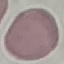

result = negative for malaria parasites
image type = cell patch, automatically extracted from a larger field of view and resized to 64 × 64 pixels
capture = smartphone camera at the microscope eyepiece
stain = Giemsa
preparation = thin blood smear